Assess for malaria.
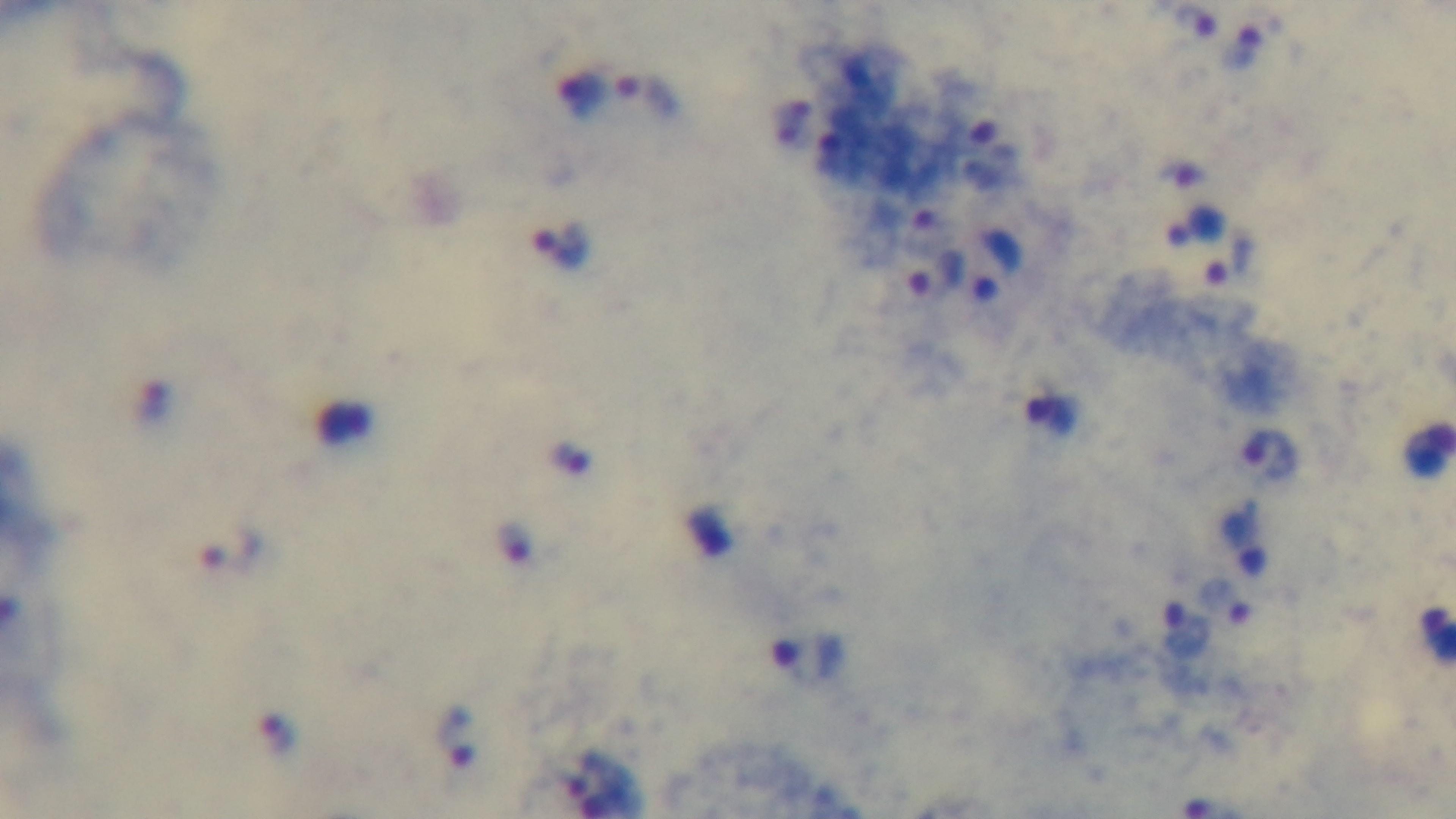
Infected.

modality = light microscopy
objective = 100x oil immersion
stain = Giemsa
field of view = single
preparation = thick
capture = mounted 4K digital camera